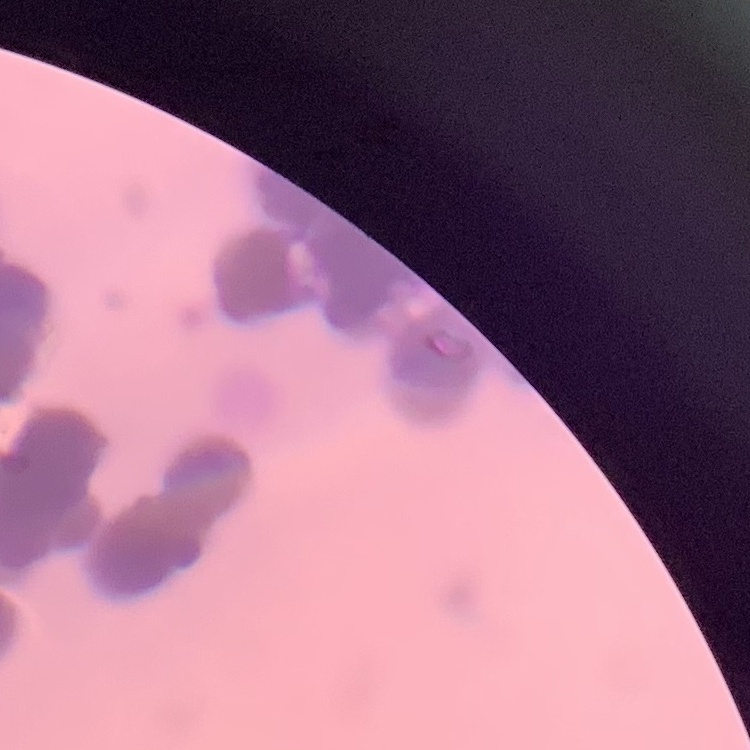
erythrocyte morphology = rouleaux formation
preparation = thin blood film
image type = square crop of a larger photomicrograph
stain = Field's or Giemsa